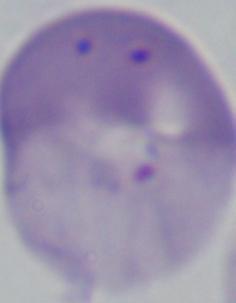

{
  "magnification": "1000x",
  "identification": "Babesia",
  "modality": "photomicrograph"
}